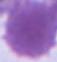
identification = red blood cell
modality = photomicrograph
magnification = 1000x